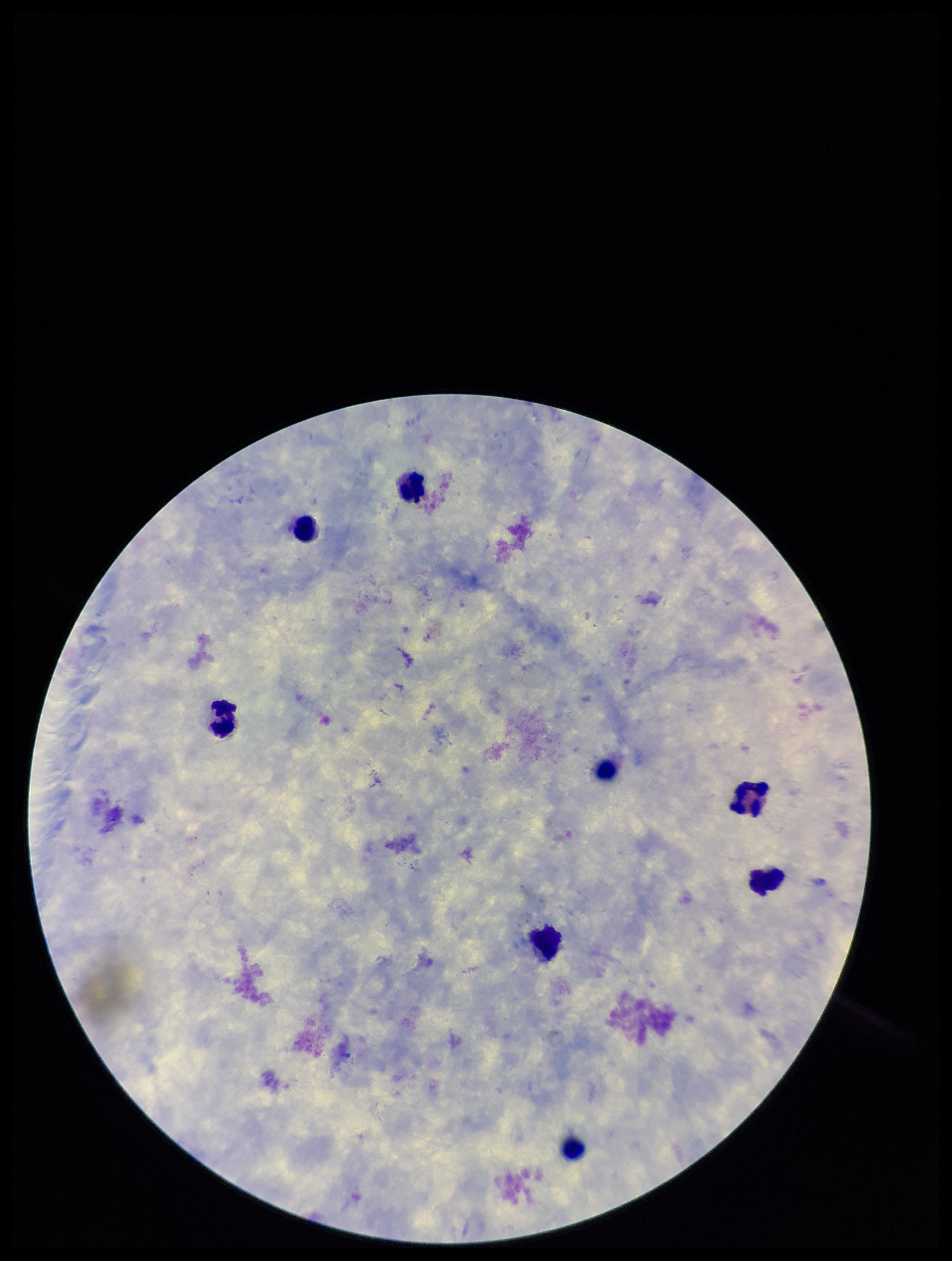
Parasite count: 0. Stained with Giemsa. Smartphone photograph taken through the eyepiece of a microscope. Plasmodium parasites: none seen. Patient malaria status: negative. One field from this slide. Image is 952×1261 pixels. Preparation: thick blood smear. Leukocyte count: 7.